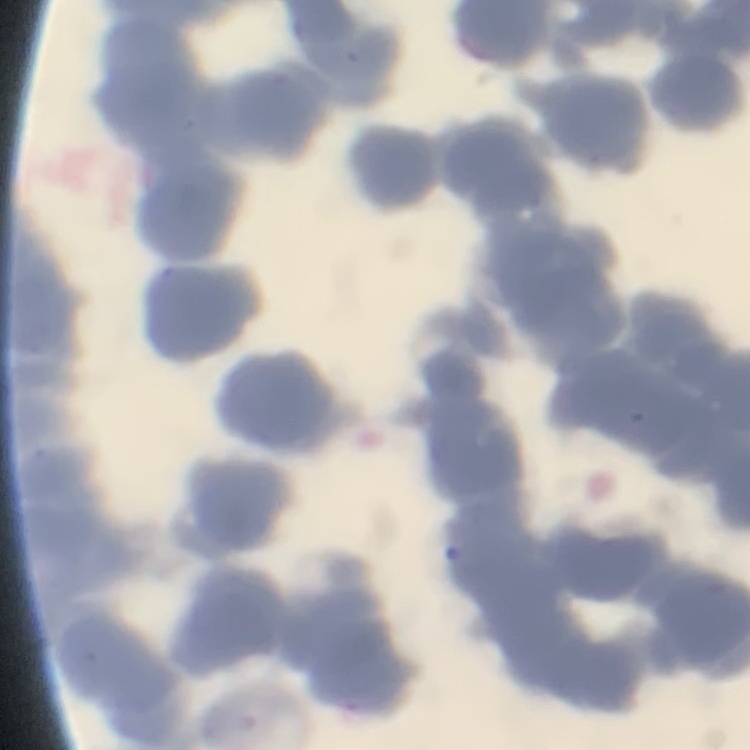
red blood cell morphology = rouleaux formation
stain = Field's or Giemsa
image type = square crop of a larger photomicrograph
preparation = thin blood film